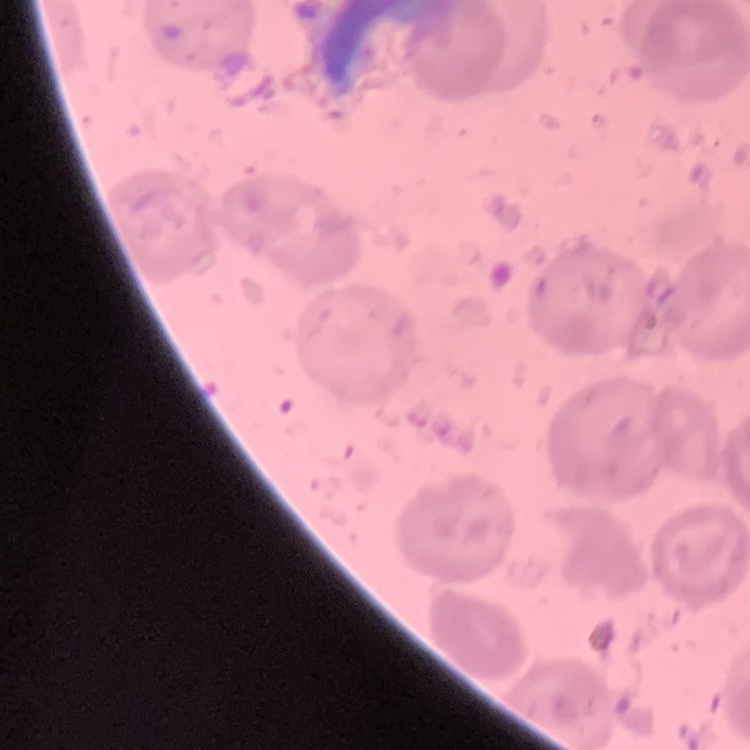

red blood cell morphology = no rouleaux formation
stain = Field's or Giemsa
image type = square crop of a larger photomicrograph
preparation = thin peripheral smear